Locate every blood parasite and identify its species.
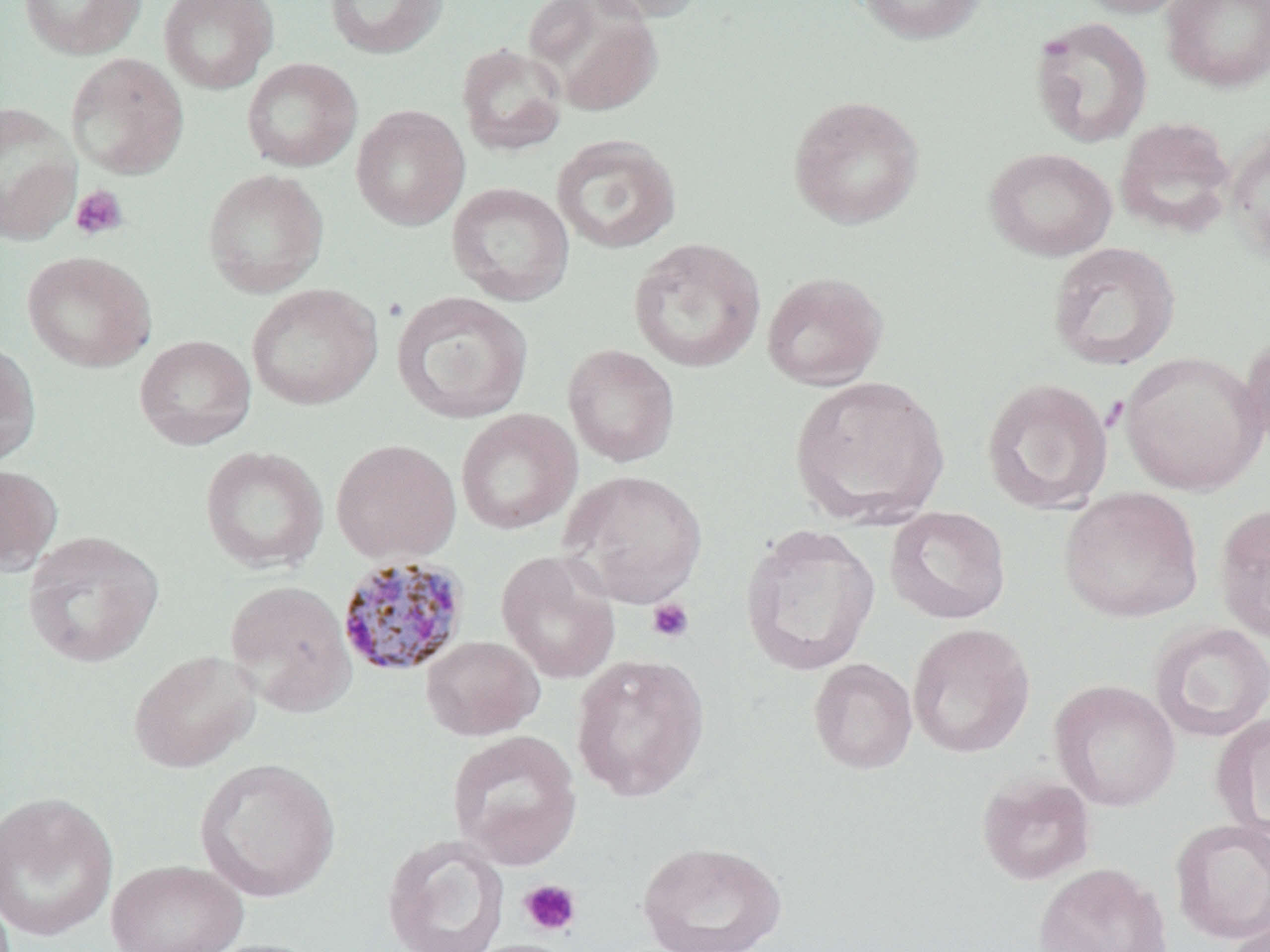
Approximate bounding boxes as (x1,y1)-(x2,y2) corner pairs in pixels.
Plasmodium malariae-infected red blood cells: (336,554)-(471,679).
No Plasmodium falciparum, Plasmodium ovale, Plasmodium vivax, Babesia divergens, or Trypanosoma brucei observed.

Summary:
  - Uninfected red blood cell locations (subset): (18,0)-(147,60), (158,0)-(279,93), (323,0)-(450,60), (524,0)-(665,117), (583,0)-(709,23), (855,0)-(988,45), (1071,0)-(1196,18), (1161,0)-(1270,93), (1029,15)-(1153,148), (456,43)-(568,157), (66,52)-(189,179), (241,58)-(362,172), (787,94)-(925,229), (0,102)-(82,244), (351,105)-(470,230), (1114,117)-(1237,239), (1224,127)-(1270,269), (551,134)-(682,254), (984,147)-(1117,262), (202,168)-(329,298), (446,182)-(575,306), (628,237)-(766,374), (1047,242)-(1181,371), (22,251)-(156,372), (761,271)-(889,391), (246,283)-(383,410), (392,291)-(534,424), (1239,331)-(1270,456), (134,335)-(256,450), (0,340)-(41,467), (562,344)-(680,467), (1119,351)-(1267,496), (789,375)-(950,528), (980,377)-(1114,514), (455,409)-(582,535), (331,439)-(461,564), (200,445)-(329,574), (0,463)-(63,575), (559,469)-(708,608), (1059,487)-(1204,623), (1214,502)-(1270,642), (884,506)-(1011,625), (739,523)-(882,676), (22,530)-(164,668), (496,549)-(621,684), (224,579)-(357,716), (1150,621)-(1270,742), (907,623)-(1035,759), (421,635)-(544,741), (128,649)-(262,774), (571,653)-(710,802), (808,658)-(917,774), (1049,679)-(1181,812), (1211,712)-(1270,842), (194,757)-(341,903), (976,772)-(1096,885), (0,791)-(120,942), (1169,818)-(1270,944), (381,834)-(511,952), (636,840)-(788,952), (105,859)-(248,952), (1033,862)-(1172,952), (1224,913)-(1270,952), (193,938)-(328,952), (460,938)-(583,952)
  - Platelet locations (subset): (70,185)-(128,241), (646,598)-(694,643), (519,879)-(582,937)
  - Slide-level diagnosis: Plasmodium malariae
  - Preparation: thin blood film
  - Field of view: one of a larger specimen
  - Modality: light microscopy
  - Magnification: 1000x
  - Image size: 1270×952 pixels
  - Stain: May-Grünwald-Giemsa